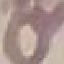

{
  "result": "negative for malaria parasites",
  "stain": "Giemsa",
  "image_type": "cell patch, automatically extracted from a larger field of view and resized to 64 × 64 pixels",
  "preparation": "thin smear",
  "capture": "smartphone through the microscope eyepiece"
}